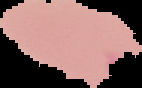

Summary:
  - Image size: 142×88 pixels
  - Preparation: thin blood smear
  - Result: negative for Plasmodium parasites
  - Image type: segmented cell region with the area outside set to black